Name the parasite shown.
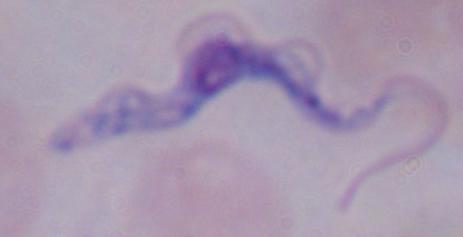
A trypanosome.

Photomicrograph. 1000x magnification.